Name the parasite shown.
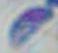

This is Toxoplasma gondii.

Summary:
  - Modality: photomicrograph
  - Magnification: 1000x